Assess this cell for malaria.
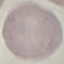

Uninfected.

Thin blood smear. Acquired by smartphone through the microscope eyepiece. Automatically extracted cell patch, resized to 64 × 64 pixels. Giemsa stain.